Name the parasite shown.
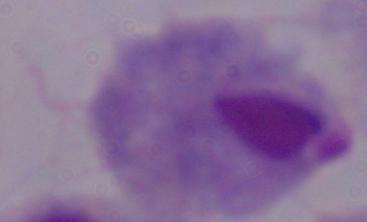
This is a trichomonad.

magnification: 1000x
modality: micrograph